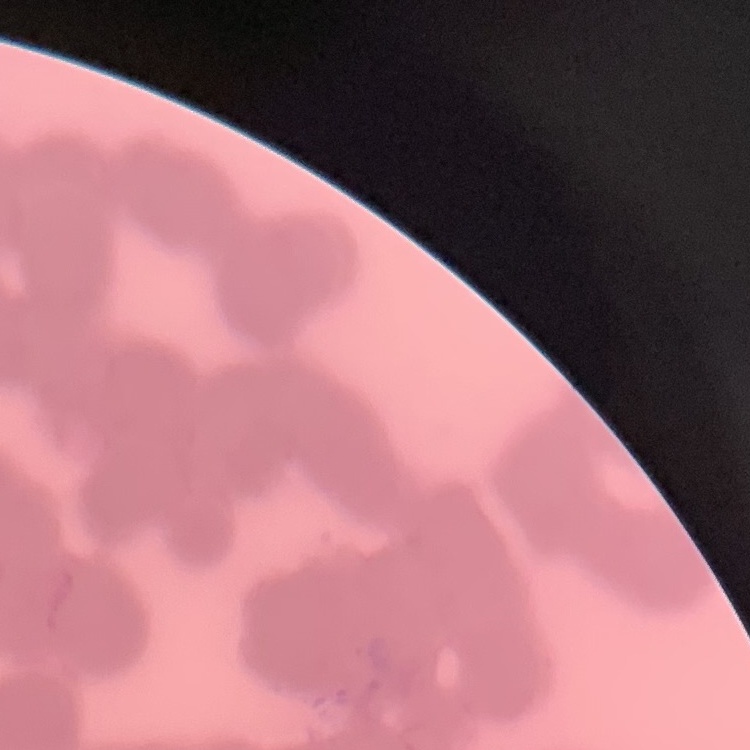
The erythrocytes exhibit rouleaux formation. Field's or Giemsa stain. Square crop of a larger photomicrograph. Thin peripheral smear.